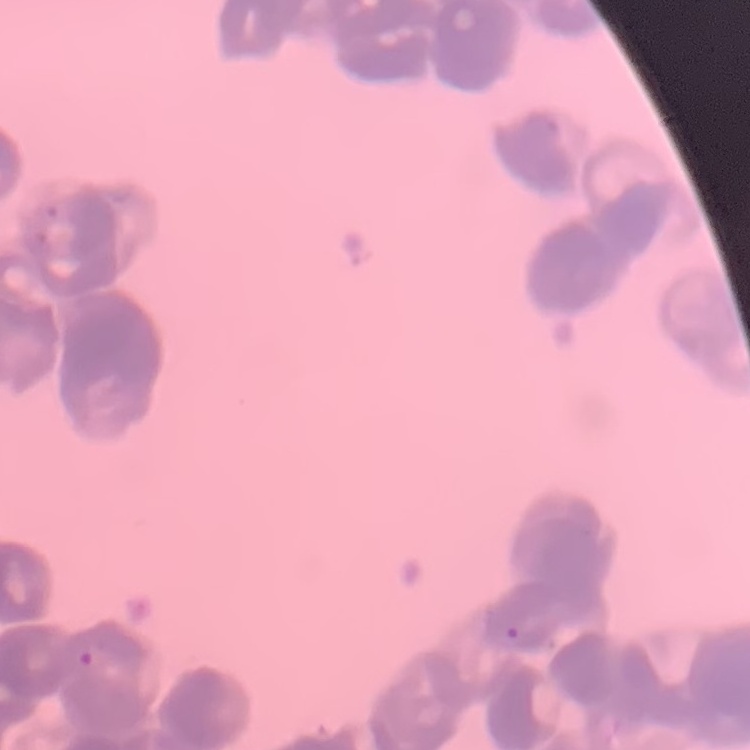

{
  "red_blood_cell_morphology": "rouleaux formation",
  "stain": "Field's or Giemsa",
  "preparation": "thin peripheral smear",
  "image_type": "square crop of a larger photomicrograph"
}